Report the malaria status of this cell.
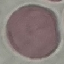
Uninfected.

Summary:
  - Capture: smartphone through the microscope eyepiece
  - Preparation: thin smear
  - Stain: Giemsa
  - Image type: automatically extracted cell patch, resized to 64 × 64 pixels